Give the position of every malaria parasite.
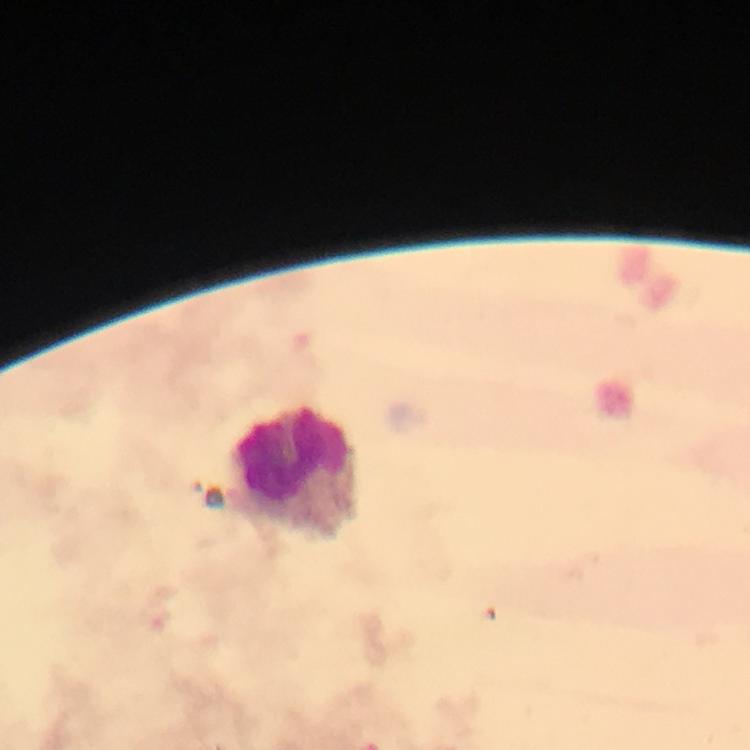

No malaria parasites detected.

immersion oil = applied
context = from a diagnostic examination for malaria
leukocyte locations = approximate centers as (x, y) in pixels: (297, 472)
image size = 750×750 pixels
magnification = 100x
capture = smartphone photograph through a microscope
preparation = thick blood film
cropped from = one field of view
stain = Giemsa